Outline each Plasmodium falciparum-infected red blood cell.
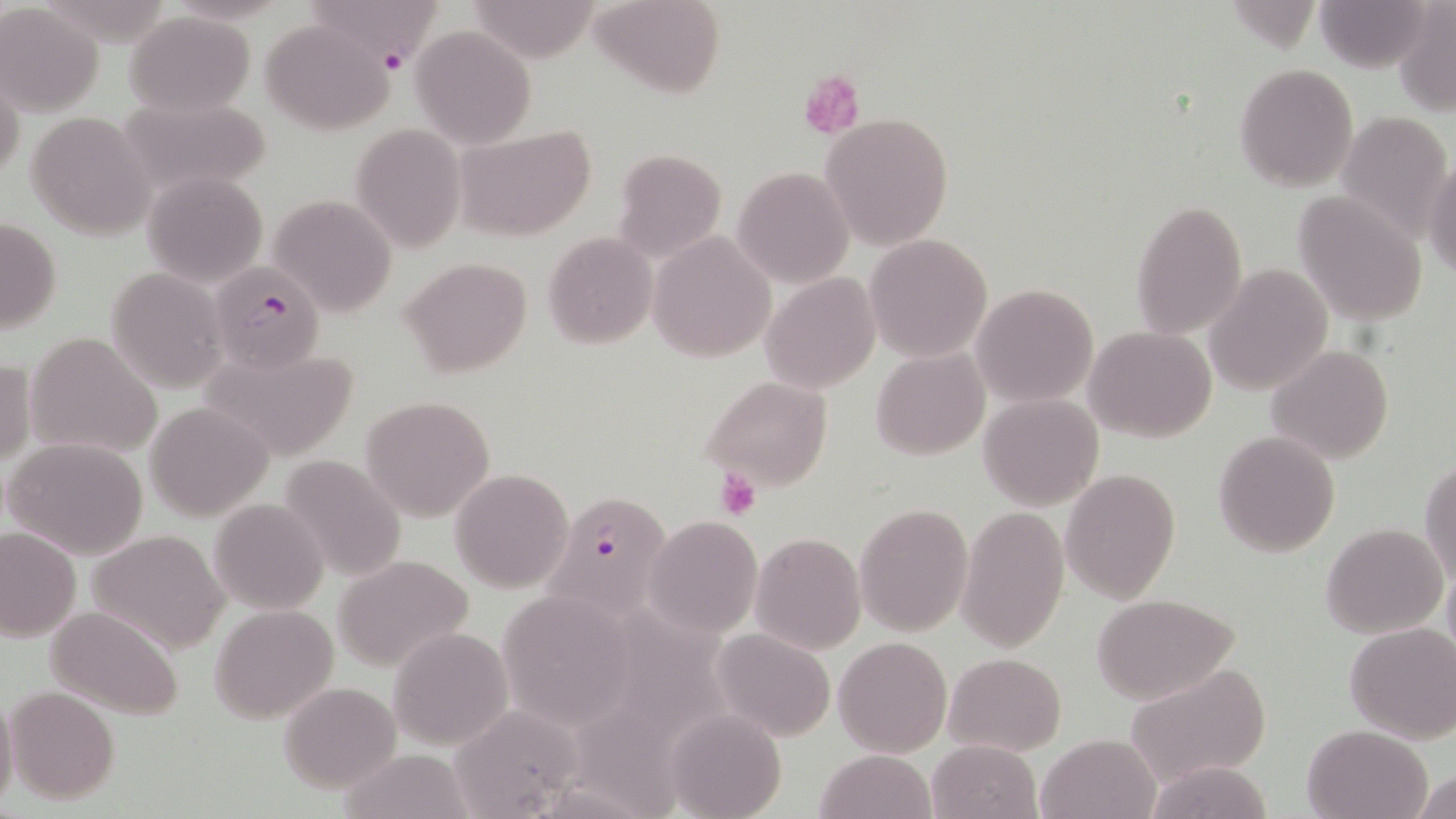
Approximate bounding boxes as named x1/y1/x2/y2 corners in pixels.
Plasmodium falciparum-infected red blood cells: (x1=306, y1=1, x2=442, y2=76), (x1=214, y1=260, x2=330, y2=385), (x1=542, y1=490, x2=676, y2=620).

slide_level_diagnosis: Plasmodium falciparum
modality: light microscopy
preparation: thin blood smear
uninfected_red_blood_cell_locations: 'approximate bounding boxes as named x1/y1/x2/y2 corners in pixels: (x1=591, y1=0, x2=726, y2=99), (x1=1316, y1=0, x2=1430, y2=72), (x1=467, y1=1, x2=603, y2=62), (x1=1393, y1=1, x2=1456, y2=119), (x1=0, y1=3, x2=101, y2=115), (x1=124, y1=11, x2=256, y2=118), (x1=259, y1=18, x2=396, y2=136), (x1=411, y1=25, x2=536, y2=149), (x1=1234, y1=62, x2=1359, y2=192), (x1=0, y1=71, x2=25, y2=189), (x1=114, y1=95, x2=273, y2=198), (x1=1336, y1=109, x2=1453, y2=242), (x1=28, y1=111, x2=153, y2=240), (x1=819, y1=112, x2=954, y2=250), (x1=351, y1=123, x2=466, y2=254), (x1=457, y1=128, x2=595, y2=242), (x1=611, y1=147, x2=726, y2=265), (x1=1423, y1=158, x2=1455, y2=281), (x1=733, y1=165, x2=854, y2=289), (x1=143, y1=171, x2=267, y2=287), (x1=1293, y1=190, x2=1427, y2=323), (x1=269, y1=193, x2=398, y2=317), (x1=1131, y1=201, x2=1247, y2=339), (x1=1, y1=215, x2=62, y2=335), (x1=649, y1=231, x2=776, y2=363), (x1=542, y1=232, x2=659, y2=350), (x1=864, y1=235, x2=992, y2=361), (x1=398, y1=257, x2=533, y2=379), (x1=1204, y1=264, x2=1332, y2=395), (x1=107, y1=267, x2=229, y2=393), (x1=760, y1=273, x2=882, y2=393), (x1=972, y1=282, x2=1097, y2=406), (x1=1085, y1=326, x2=1218, y2=443), (x1=28, y1=331, x2=163, y2=460), (x1=197, y1=342, x2=362, y2=461), (x1=1267, y1=345, x2=1393, y2=465), (x1=872, y1=348, x2=989, y2=461), (x1=1, y1=358, x2=33, y2=471), (x1=702, y1=375, x2=833, y2=494), (x1=978, y1=394, x2=1102, y2=510), (x1=360, y1=395, x2=494, y2=519), (x1=143, y1=401, x2=272, y2=519), (x1=1213, y1=430, x2=1341, y2=557), (x1=4, y1=437, x2=149, y2=559), (x1=276, y1=453, x2=409, y2=581), (x1=1421, y1=460, x2=1455, y2=587), (x1=450, y1=468, x2=575, y2=594), (x1=1060, y1=468, x2=1180, y2=603), (x1=209, y1=498, x2=328, y2=613), (x1=855, y1=501, x2=974, y2=638), (x1=956, y1=505, x2=1070, y2=653), (x1=645, y1=516, x2=761, y2=638), (x1=1321, y1=523, x2=1447, y2=638), (x1=0, y1=527, x2=80, y2=642), (x1=87, y1=528, x2=232, y2=656), (x1=751, y1=533, x2=866, y2=655), (x1=330, y1=553, x2=477, y2=673), (x1=503, y1=590, x2=626, y2=719), (x1=1088, y1=592, x2=1241, y2=705), (x1=44, y1=604, x2=186, y2=721), (x1=210, y1=604, x2=338, y2=723), (x1=593, y1=605, x2=747, y2=724), (x1=1344, y1=622, x2=1456, y2=744), (x1=389, y1=627, x2=512, y2=750), (x1=712, y1=628, x2=836, y2=744), (x1=833, y1=637, x2=952, y2=757), (x1=943, y1=652, x2=1066, y2=756), (x1=1122, y1=665, x2=1272, y2=788), (x1=278, y1=680, x2=402, y2=791), (x1=6, y1=686, x2=121, y2=805), (x1=0, y1=691, x2=19, y2=814), (x1=566, y1=696, x2=688, y2=819), (x1=447, y1=704, x2=589, y2=818), (x1=665, y1=708, x2=786, y2=819), (x1=1302, y1=724, x2=1432, y2=819), (x1=1036, y1=732, x2=1161, y2=819), (x1=926, y1=739, x2=1044, y2=819), (x1=339, y1=749, x2=478, y2=819), (x1=813, y1=749, x2=936, y2=819), (x1=1142, y1=759, x2=1278, y2=819), (x1=1412, y1=768, x2=1455, y2=819)'
field_of_view: single
magnification: 1000x
platelet_locations: 'approximate bounding boxes as named x1/y1/x2/y2 corners in pixels: (x1=799, y1=71, x2=866, y2=138), (x1=715, y1=470, x2=762, y2=520)'
stain: May-Grünwald-Giemsa
image_size: 1456×819 pixels